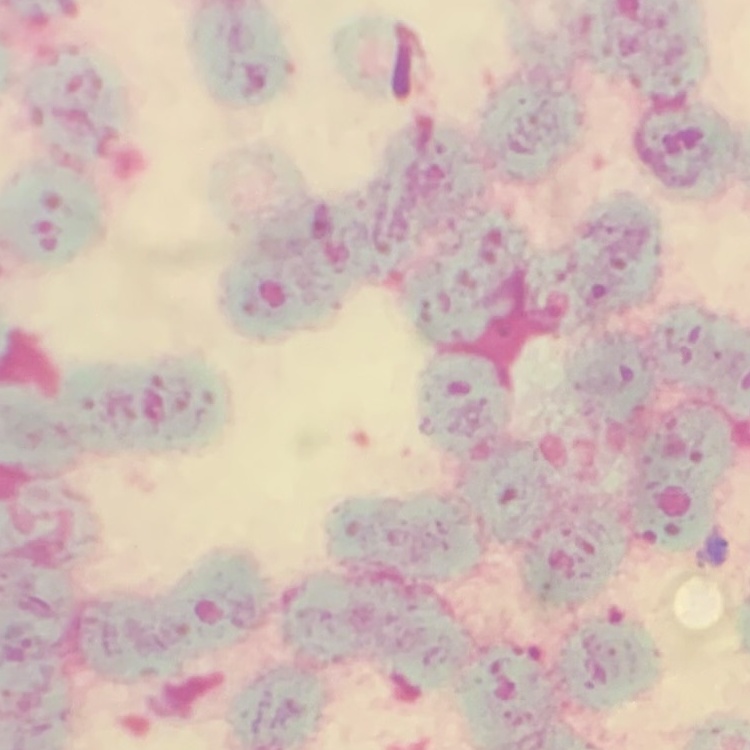
The red blood cells show rouleaux formation. Thin peripheral smear. Square crop of a larger photomicrograph. Stained with either Field's or Giemsa.